Report the malaria status of this cell.
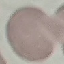

Uninfected.

Automatically extracted cell patch, resized to 64 × 64 pixels. Thin smear of blood. Acquired by smartphone through the microscope eyepiece. Giemsa stain.